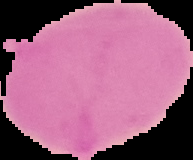
Summary:
  - Preparation: thin blood film
  - Malaria status: uninfected
  - Image type: segmented cell region on a black background
  - Image size: 193×160 pixels